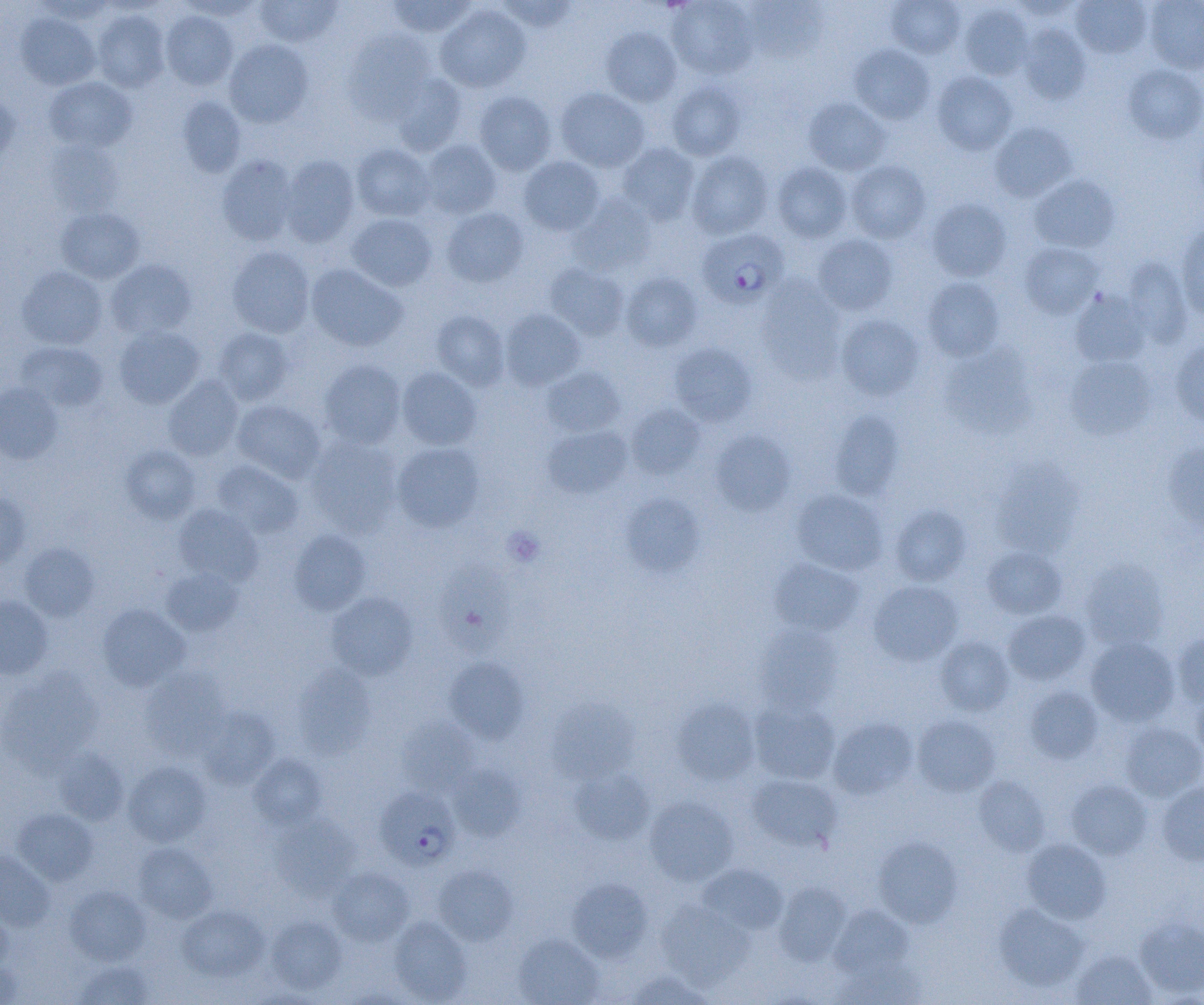 Approximate bounding boxes as (x1, y1, x2, y2) in pixels. Plasmodium falciparum-infected red blood cell locations: (697, 228, 789, 309), (375, 787, 459, 871). Platelet locations: (502, 526, 545, 567). Uninfected red blood cell locations: (176, 0, 264, 21), (387, 0, 477, 37), (667, 0, 757, 79), (886, 0, 964, 58), (1008, 0, 1086, 21), (1071, 0, 1152, 58), (1145, 0, 1204, 74), (254, 1, 343, 47), (495, 1, 578, 32), (742, 1, 824, 63), (958, 3, 1032, 80), (436, 4, 531, 93), (92, 9, 170, 92), (160, 11, 238, 90), (15, 12, 100, 90), (1018, 24, 1090, 104), (601, 27, 682, 107), (342, 29, 435, 122), (224, 39, 313, 127), (849, 44, 934, 124), (1122, 64, 1204, 144), (932, 71, 1017, 155), (391, 74, 467, 156), (44, 77, 137, 152), (666, 80, 747, 160), (555, 87, 650, 172), (473, 91, 556, 175), (0, 94, 19, 171), (176, 96, 246, 177), (803, 98, 890, 175), (990, 122, 1076, 201), (45, 140, 124, 217), (420, 141, 502, 218), (618, 142, 700, 224), (351, 144, 434, 221), (686, 151, 774, 239), (216, 154, 298, 245), (280, 155, 360, 247), (518, 156, 605, 235), (846, 160, 931, 243), (771, 162, 853, 243), (1029, 174, 1119, 253), (570, 194, 657, 276), (926, 198, 1011, 281), (56, 207, 145, 283), (441, 207, 529, 287), (347, 214, 437, 291), (1175, 224, 1204, 320), (813, 234, 898, 316), (1019, 242, 1104, 318), (227, 245, 314, 338), (1121, 258, 1193, 347), (106, 259, 196, 339), (545, 263, 629, 340), (306, 264, 408, 352), (17, 266, 107, 349), (620, 272, 703, 352), (922, 277, 1004, 360), (757, 278, 847, 385), (1071, 289, 1152, 367), (500, 309, 585, 390), (431, 310, 509, 391), (836, 315, 924, 401), (114, 325, 205, 409), (213, 328, 294, 406), (1170, 337, 1204, 431), (15, 342, 109, 412), (669, 342, 757, 426), (940, 346, 1036, 440), (1064, 356, 1157, 440), (319, 359, 406, 449), (396, 367, 482, 450), (541, 367, 625, 437), (163, 376, 244, 461), (0, 382, 63, 464), (233, 400, 326, 483), (625, 404, 706, 480), (830, 410, 904, 500), (542, 425, 633, 499), (710, 430, 795, 515), (306, 437, 402, 537), (1163, 440, 1204, 533), (392, 442, 485, 532), (120, 445, 201, 524), (990, 459, 1081, 558), (212, 460, 303, 538), (791, 488, 888, 575), (0, 492, 31, 567), (621, 494, 704, 577), (173, 504, 263, 586), (889, 504, 972, 586), (288, 529, 371, 615), (19, 543, 100, 621), (982, 546, 1066, 619), (440, 557, 515, 656), (769, 558, 864, 636), (1079, 559, 1171, 651), (161, 567, 243, 636), (868, 580, 963, 666), (326, 591, 418, 681), (0, 596, 53, 679), (98, 604, 190, 691), (1003, 610, 1090, 685), (754, 623, 844, 713), (1172, 631, 1204, 709), (935, 635, 1014, 716), (1085, 637, 1180, 726), (445, 657, 530, 743), (292, 664, 376, 760), (141, 666, 231, 760), (0, 669, 103, 772), (1191, 684, 1204, 762), (1024, 686, 1103, 763), (548, 698, 638, 783), (673, 698, 760, 786), (749, 699, 840, 784), (198, 707, 280, 789), (912, 715, 999, 796), (396, 717, 479, 796), (828, 717, 918, 800), (1120, 722, 1204, 802), (54, 748, 128, 825), (248, 753, 327, 830), (123, 761, 212, 846), (448, 765, 525, 841), (569, 766, 654, 844), (747, 774, 842, 852), (974, 776, 1049, 855), (1066, 778, 1152, 859), (1157, 782, 1204, 866), (645, 796, 738, 885), (13, 808, 98, 884), (270, 813, 360, 898), (873, 836, 963, 927), (1022, 839, 1111, 924), (133, 843, 217, 923), (0, 850, 55, 931), (698, 864, 788, 934), (434, 865, 518, 945), (329, 867, 414, 946), (568, 878, 653, 962), (773, 881, 851, 966), (64, 885, 150, 965), (656, 900, 754, 988), (994, 903, 1090, 991), (177, 904, 269, 981), (830, 904, 912, 978), (0, 908, 13, 977), (1135, 915, 1204, 998), (265, 916, 348, 993), (389, 916, 471, 1004), (513, 933, 604, 1005), (1071, 949, 1157, 1005), (833, 958, 926, 1004), (0, 959, 23, 1005), (74, 960, 155, 1005), (623, 969, 716, 1004). Slide-level diagnosis: Plasmodium falciparum. Captured at 1000x magnification. Thin blood smear. Image is 1204×1005 pixels. Single field of view. Light microscopy.